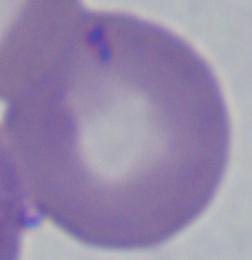

Photomicrograph. A Babesia parasite is shown. 1000x magnification.